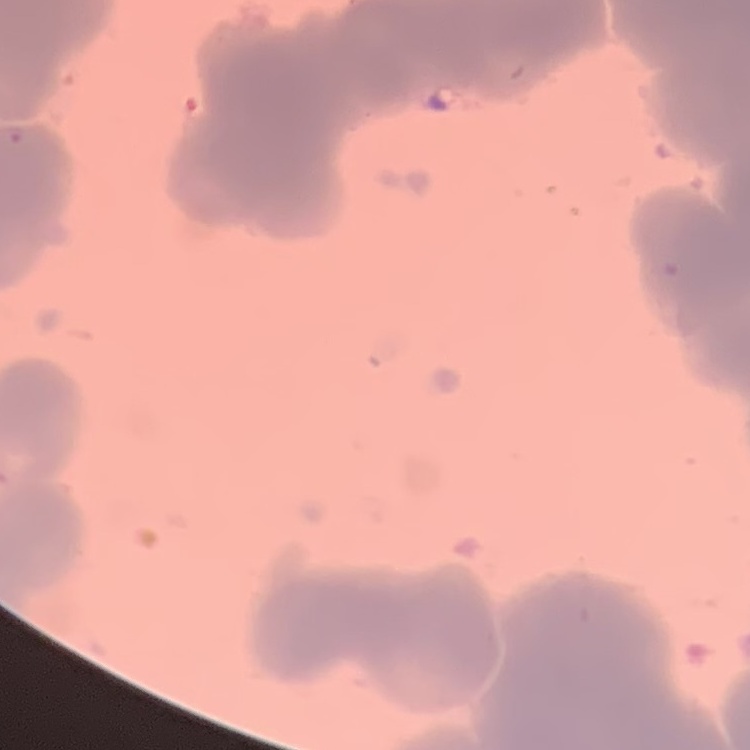

erythrocyte morphology = rouleaux formation
image type = one tile cut from a larger photomicrograph
preparation = thin peripheral smear
stain = Field's or Giemsa